Assess for malaria.
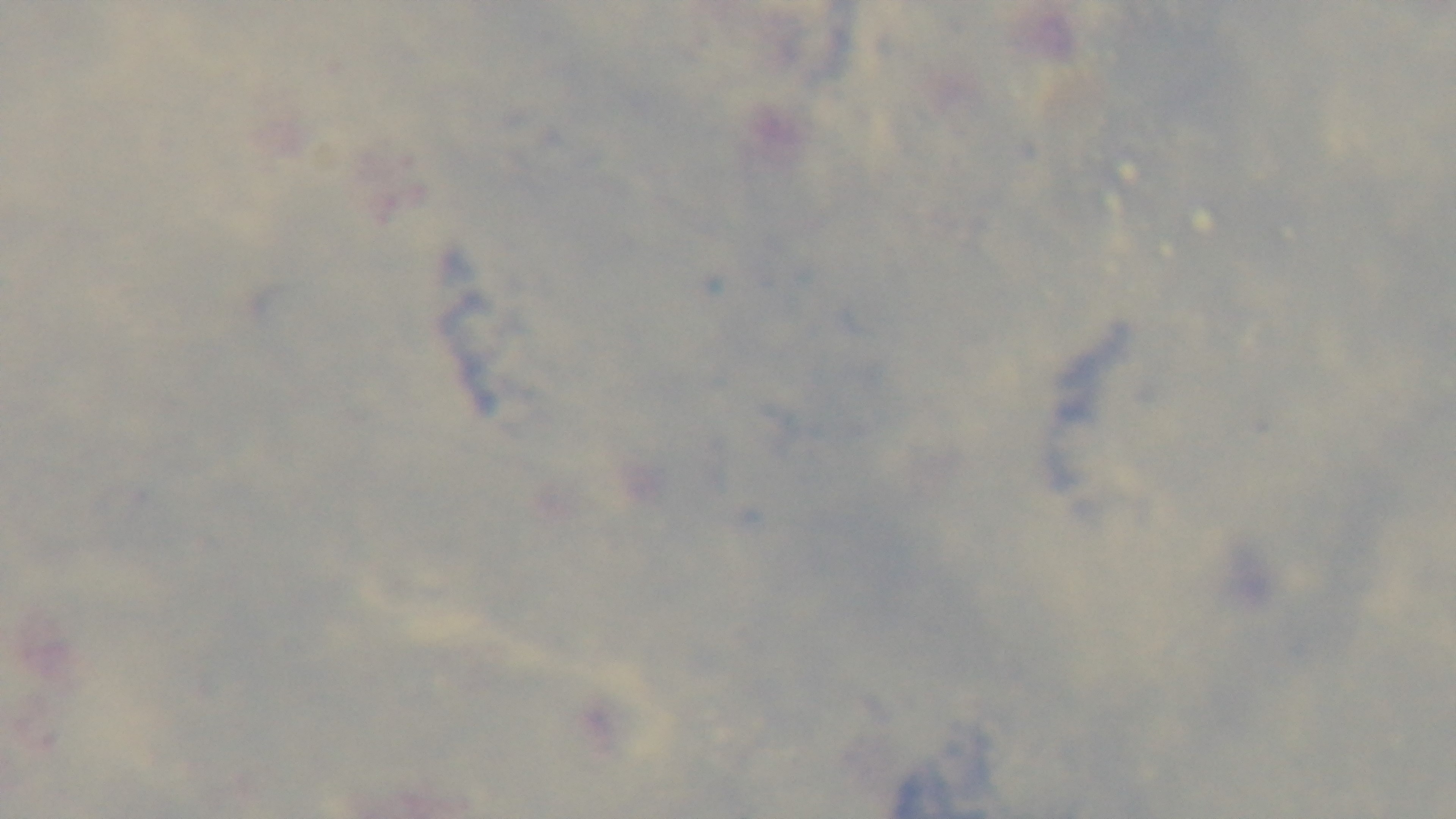

Negative.

100x oil-immersion objective. Preparation: thick. One field from the slide. Giemsa-stained. Photomicrograph. Captured with a mounted 4K digital camera.